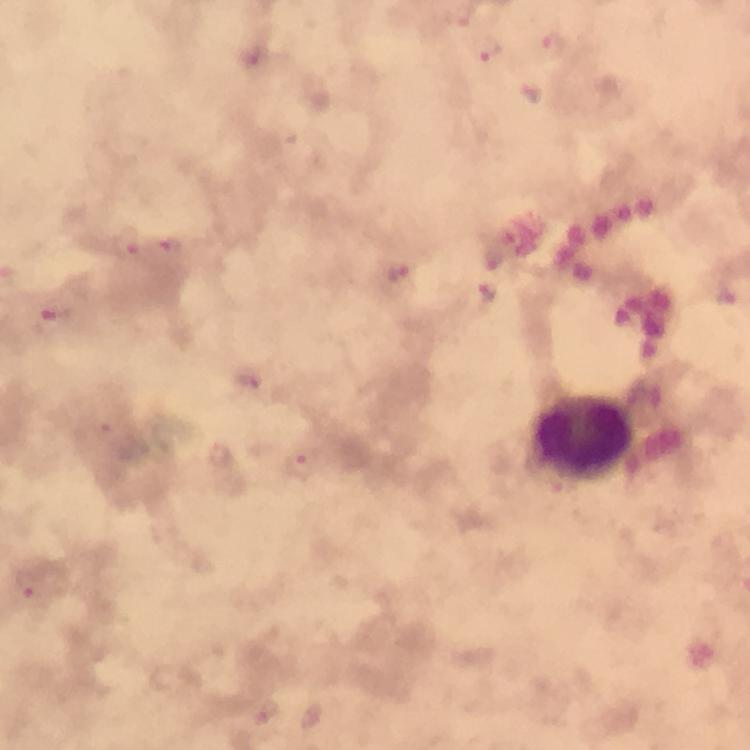

Approximate object centers, in pixels from the top-left corner. Leukocyte locations: (x=585, y=440). Malaria parasite locations: (x=552, y=46), (x=487, y=51), (x=252, y=57), (x=530, y=92), (x=128, y=244), (x=173, y=248), (x=397, y=273), (x=486, y=291), (x=728, y=295), (x=56, y=313), (x=249, y=380), (x=218, y=455), (x=302, y=464), (x=30, y=584), (x=265, y=712), (x=314, y=716). Thick smear. Giemsa stain. 100x magnification. Photographed through the microscope with a smartphone camera. Image is 750×750 pixels. Immersion oil applied. A crop from one field of view. From a diagnostic examination for malaria.